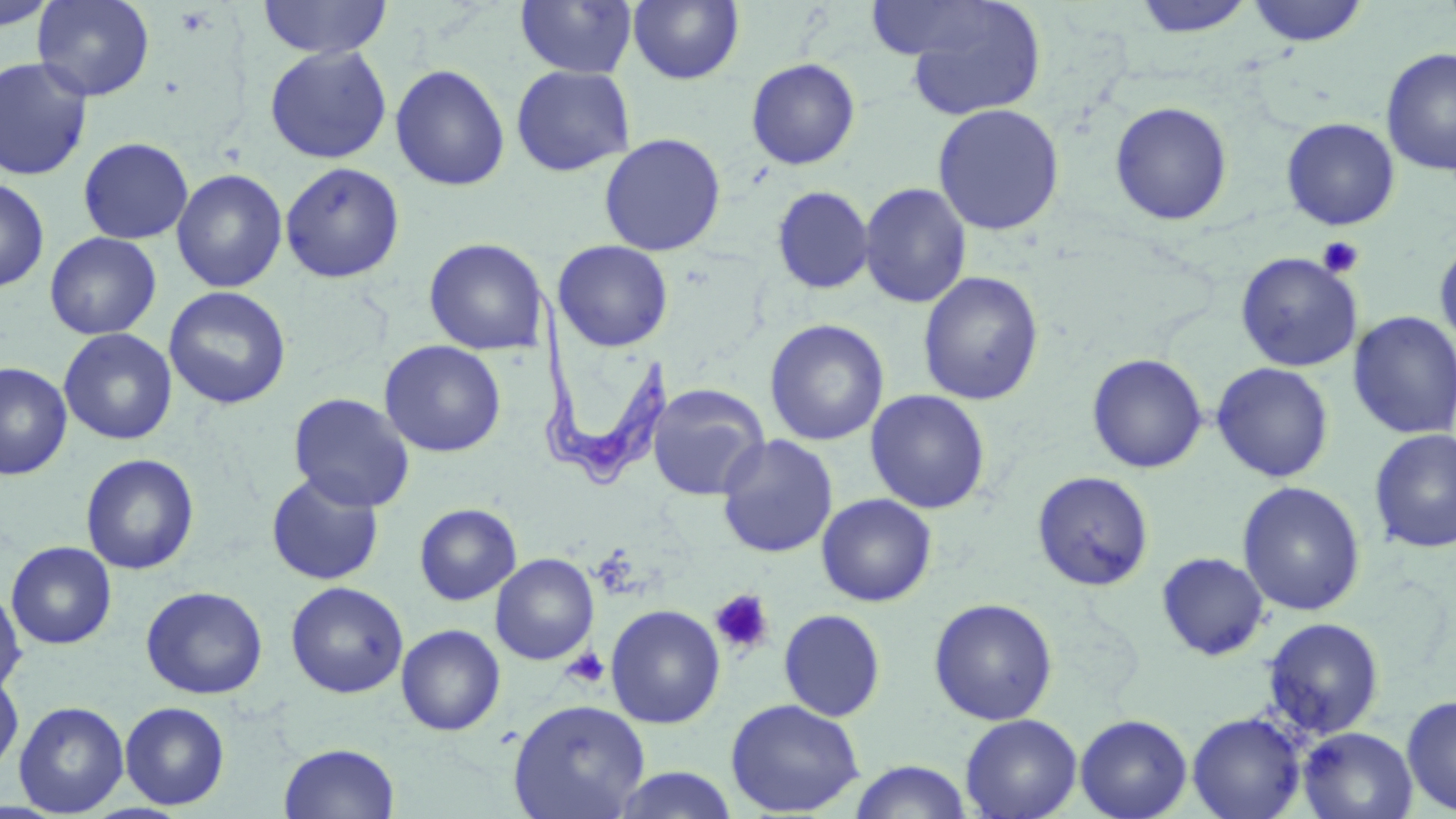
Summary:
  - Coordinate format: approximate bounding boxes as (x1, y1, x2, y2) in pixels
  - Uninfected red blood cell locations: (0, 0, 58, 33), (32, 0, 155, 102), (257, 0, 392, 60), (514, 0, 638, 78), (627, 0, 744, 85), (864, 0, 1000, 61), (1130, 0, 1257, 39), (1245, 0, 1369, 47), (903, 2, 1046, 121), (265, 45, 392, 164), (1381, 47, 1456, 177), (0, 57, 93, 181), (745, 57, 861, 170), (390, 63, 511, 191), (510, 65, 636, 177), (1110, 101, 1233, 226), (931, 104, 1065, 235), (1280, 117, 1400, 230), (599, 132, 726, 256), (78, 137, 193, 244), (280, 162, 405, 283), (171, 169, 288, 293), (0, 176, 49, 293), (859, 182, 972, 308), (771, 186, 874, 294), (44, 232, 162, 340), (423, 237, 550, 356), (1434, 238, 1456, 353), (553, 240, 673, 351), (1235, 252, 1362, 372), (918, 271, 1044, 405), (163, 286, 292, 410), (1348, 310, 1456, 439), (764, 319, 888, 446), (58, 328, 177, 446), (379, 340, 506, 458), (1086, 353, 1208, 474), (0, 361, 72, 480), (1211, 362, 1334, 483), (646, 383, 770, 501), (865, 389, 990, 514), (287, 391, 415, 512), (1369, 429, 1456, 554), (716, 433, 839, 558), (80, 453, 199, 575), (1032, 470, 1154, 591), (266, 472, 385, 586), (1237, 481, 1365, 616), (816, 493, 937, 607), (414, 503, 522, 605), (5, 542, 118, 649), (1156, 552, 1270, 661), (490, 553, 599, 665), (285, 581, 409, 699), (140, 585, 267, 699), (0, 586, 27, 696), (928, 598, 1058, 725), (605, 604, 726, 728), (778, 609, 886, 721), (1262, 616, 1385, 738), (396, 624, 505, 736), (0, 672, 24, 776), (1401, 694, 1456, 815), (725, 698, 865, 816), (507, 699, 650, 819), (14, 701, 129, 816), (120, 701, 230, 810), (1187, 712, 1306, 819), (960, 713, 1082, 819), (1074, 714, 1193, 819), (1298, 727, 1417, 819), (279, 742, 400, 819), (848, 760, 974, 819), (609, 766, 741, 818)
  - Trypanosoma brucei locations: (528, 287, 670, 488)
  - Platelet locations: (1317, 235, 1364, 279), (709, 589, 774, 656), (561, 647, 609, 689)
  - Slide-level diagnosis: Trypanosoma brucei
  - Stain: May-Grünwald-Giemsa
  - Image size: 1456×819 pixels
  - Preparation: thin blood film
  - Field of view: single
  - Magnification: 1000x
  - Modality: optical microscopy